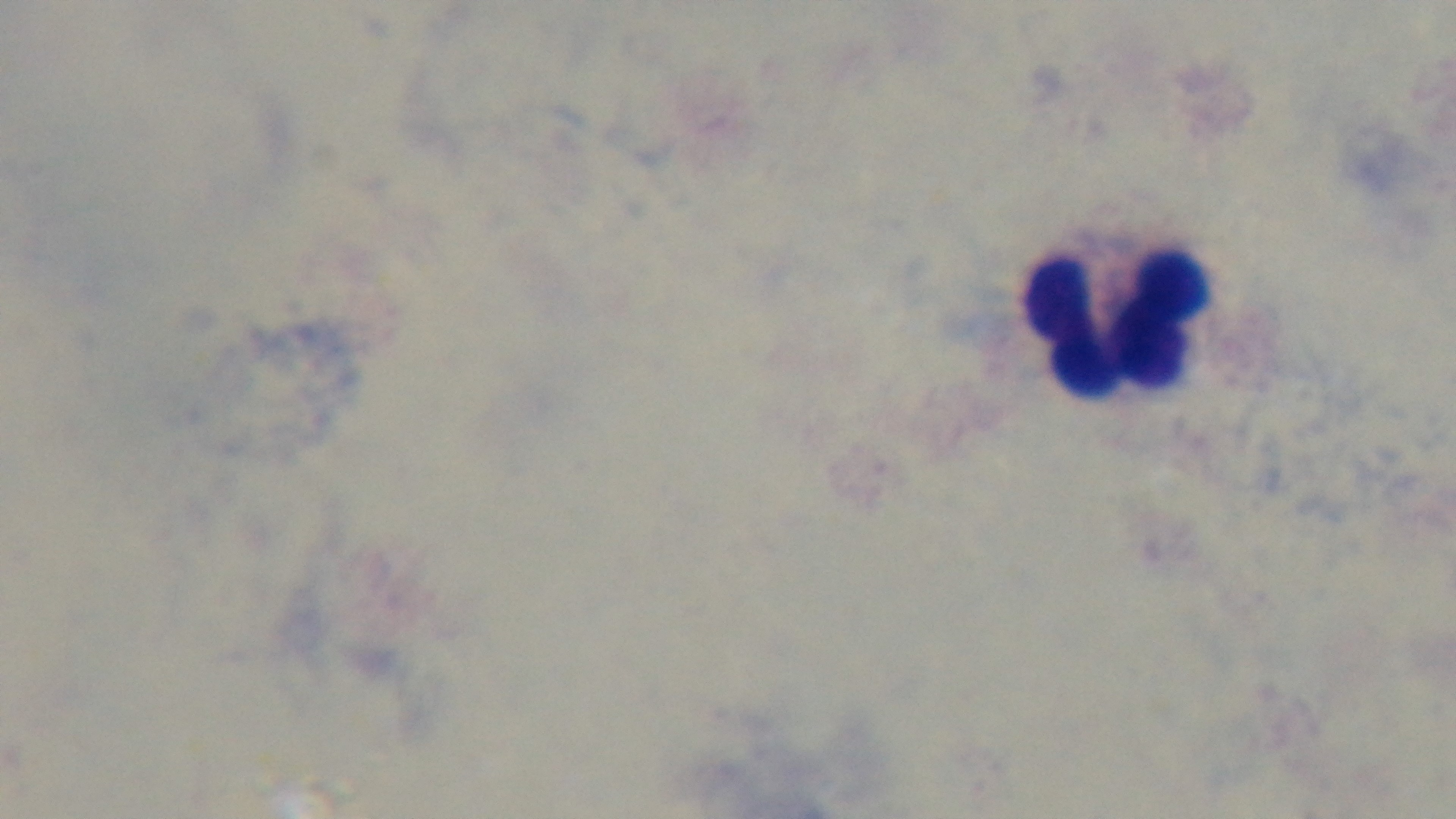

Summary:
  - Capture: mounted 4K digital camera
  - Field of view: single
  - Preparation: thick
  - Stain: Giemsa
  - Malaria status: negative
  - Modality: light microscopy
  - Objective: 100x oil immersion